Point out each leukocyte.
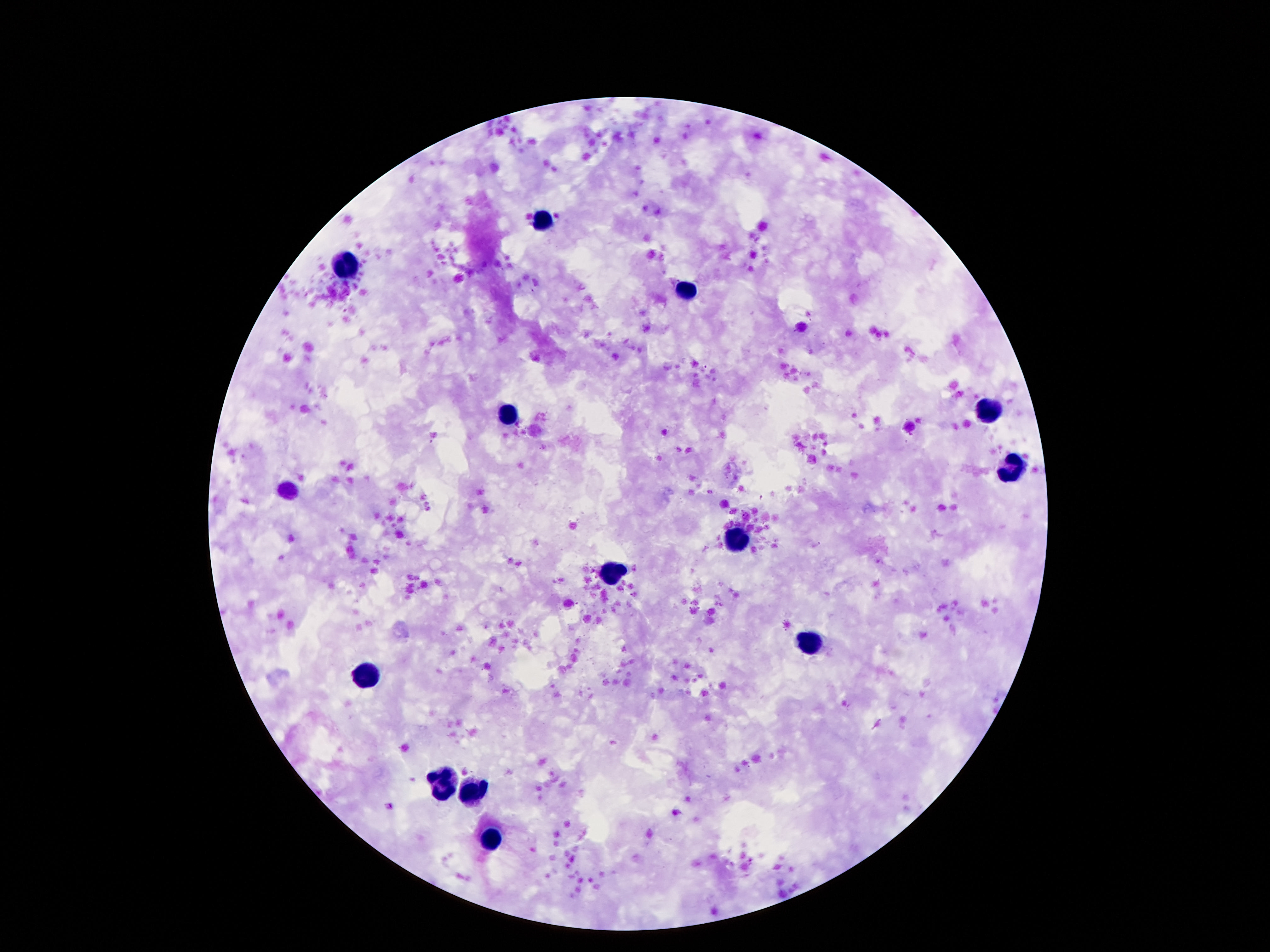
Approximate centers as [x, y] in pixels.
Leukocytes: [543, 219], [346, 266], [688, 291], [989, 412], [508, 417], [1012, 467], [739, 541], [612, 572], [809, 643], [365, 674], [444, 781], [475, 793], [490, 839].

Photographed through the microscope eyepiece with a smartphone camera. Patient malaria status: not infected. 100x magnification. Thick blood film. Image is 1270×952 pixels. Single field of view. Giemsa-stained preparation.